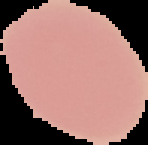 From a thin blood smear. The area outside the segmented cell region is set to black. Image is 148×145 pixels. Malaria status: uninfected.